Assess this cell for malaria.
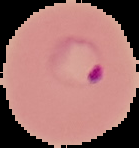
Parasitized.

From a thin blood smear. Segmented cell region on a black background. Image is 139×148 pixels.